Report the malaria status of this cell.
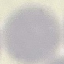
Uninfected.

Acquired by smartphone through the microscope eyepiece. Thin blood smear. Giemsa-stained preparation. Cell patch, automatically extracted from a larger field of view and resized to 64 × 64 pixels.